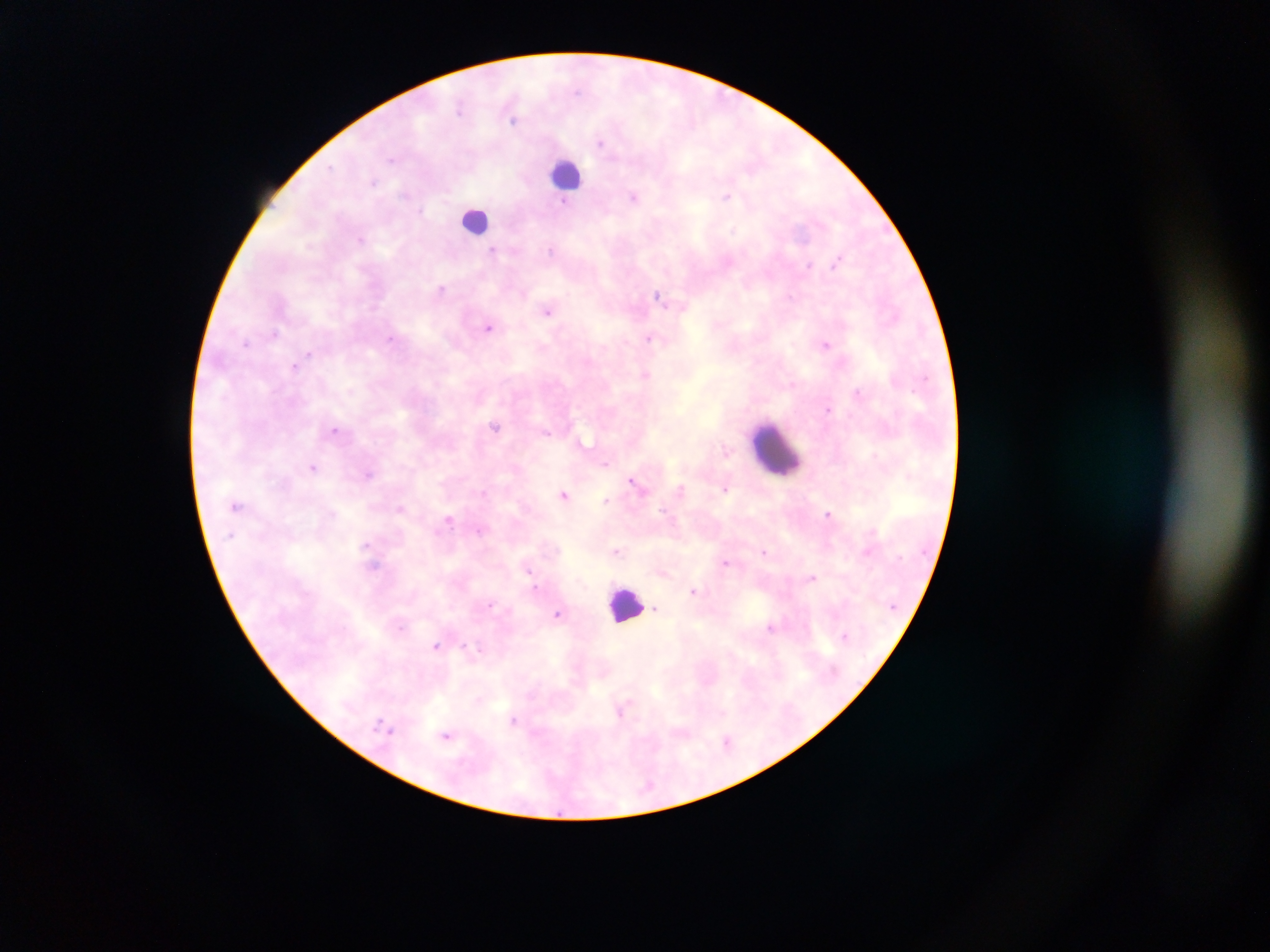

capture = mobile-phone photograph through a microscope
field of view = single
malaria parasite locations = approximate centers as x y in pixels: 514 120; 600 141; 727 196; 634 197; 362 239; 494 251; 839 260; 442 289; 660 298; 549 310; 489 327; 274 333; 649 338; 826 344; 295 365; 646 375; 830 408; 495 426; 337 430; 726 453; 606 462; 313 467; 369 474; 634 483; 725 487; 680 490; 565 494; 606 500; 237 506; 401 508; 830 513; 449 518; 617 551; 765 551; 726 563; 372 564; 662 571; 812 576; 695 591; 490 606; 658 609; 559 613; 401 626; 772 627; 845 635; 437 647; 468 647; 623 709; 514 720; 447 735; 728 741
country = Ghana
preparation = thick blood film
image size = 1270×952 pixels
leukocyte locations = approximate centers as x y in pixels: 567 173; 476 219; 774 449; 626 604